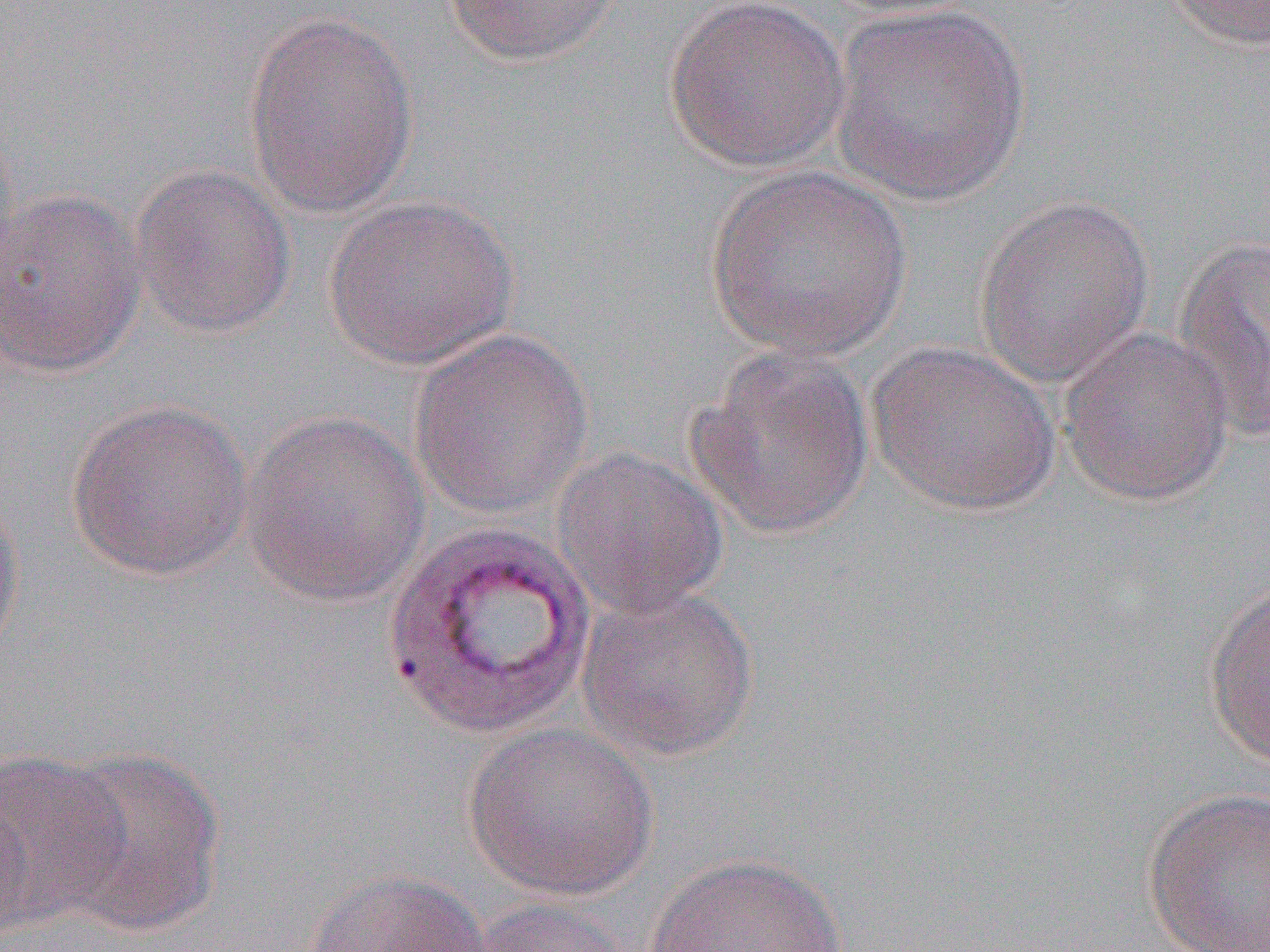 Approximate bounding boxes as [x1, y1, x2, y2] in pixels. Uninfected red blood cell locations (subset): [442, 0, 627, 67], [663, 0, 849, 174], [812, 0, 987, 18], [1155, 0, 1270, 50], [828, 4, 1032, 207], [243, 12, 419, 218], [128, 163, 297, 339], [704, 164, 912, 360], [1, 186, 147, 379], [322, 194, 519, 370], [973, 195, 1155, 390], [1169, 236, 1270, 443], [408, 326, 594, 519], [1058, 327, 1234, 504], [867, 340, 1062, 516], [686, 346, 876, 541], [64, 398, 255, 581], [240, 409, 432, 607], [551, 445, 730, 619], [0, 487, 25, 664], [1203, 577, 1270, 773], [576, 584, 760, 761], [462, 722, 659, 901], [48, 746, 227, 935], [0, 751, 129, 932], [0, 786, 34, 947], [1142, 787, 1270, 952], [644, 852, 849, 952], [305, 868, 493, 952], [465, 896, 637, 952]. Slide-level diagnosis: Plasmodium vivax. Image is 1270×952 pixels. Light microscopy. 1000x magnification. Thin blood film. Single field of view.